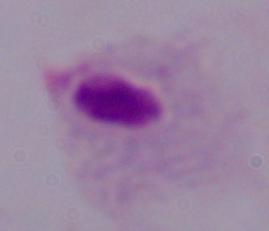

identification = trichomonad
modality = micrograph
magnification = 1000x